Classify this cell by malaria status.
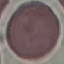

Uninfected.

Summary:
  - Preparation: thin smear
  - Image type: automatically extracted cell patch, resized to 64 × 64 pixels
  - Stain: Giemsa
  - Capture: smartphone camera at the microscope eyepiece